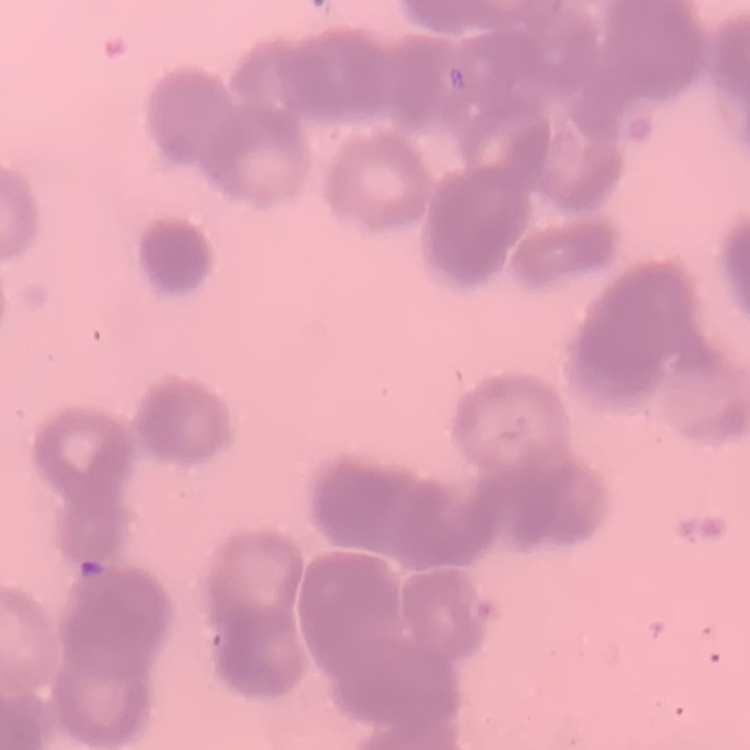 The red blood cells exhibit rouleaux formation. One tile cut from a larger photomicrograph. Stained with either Field's or Giemsa. Thin peripheral smear.